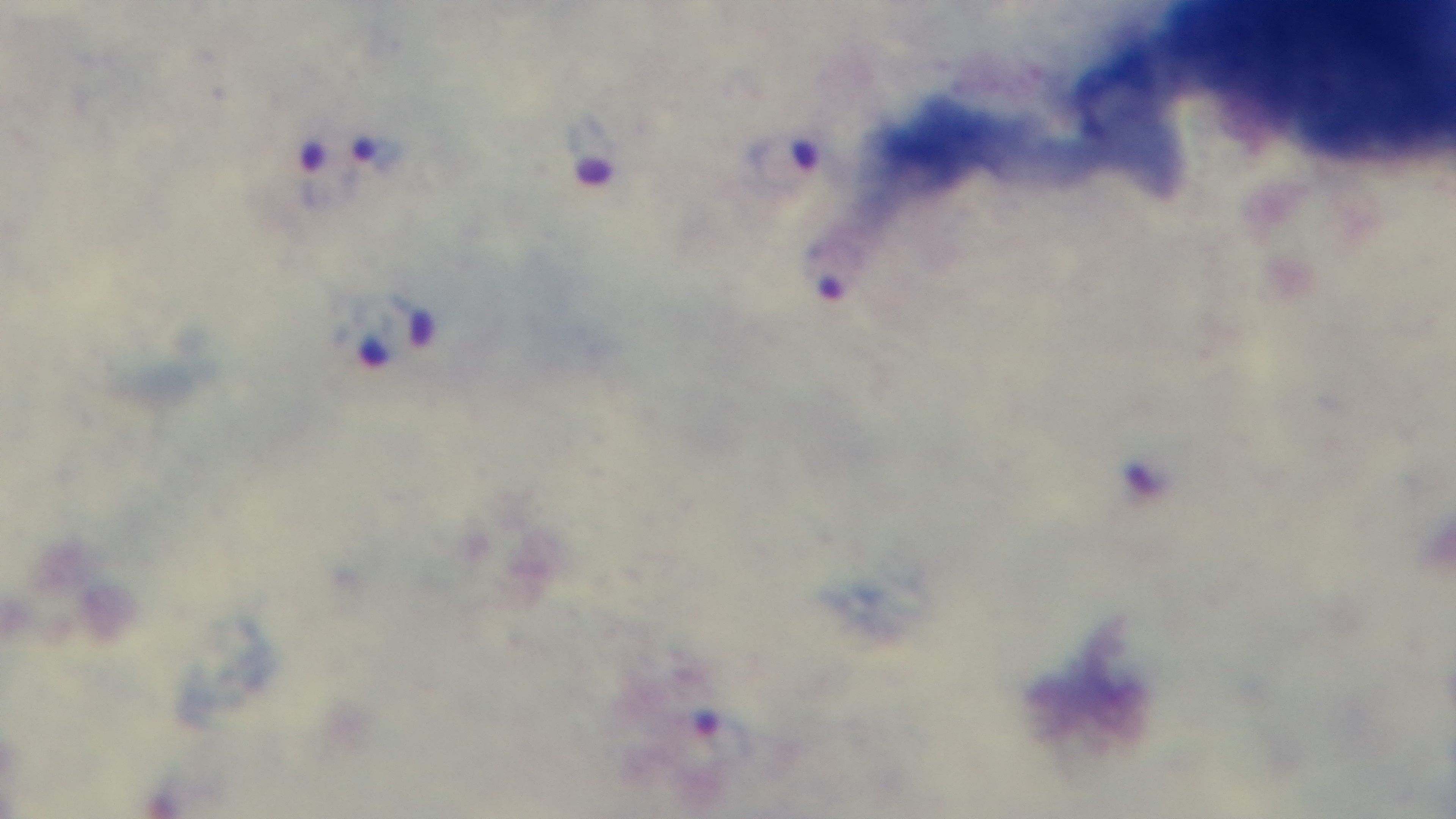
Summary:
  - Stain: Giemsa
  - Preparation: thick blood film
  - Capture: mounted 4K digital camera
  - Objective: 100x oil immersion
  - Field of view: one from the slide
  - Malaria status: positive
  - Modality: light microscopy